Locate every blood parasite and identify its species.
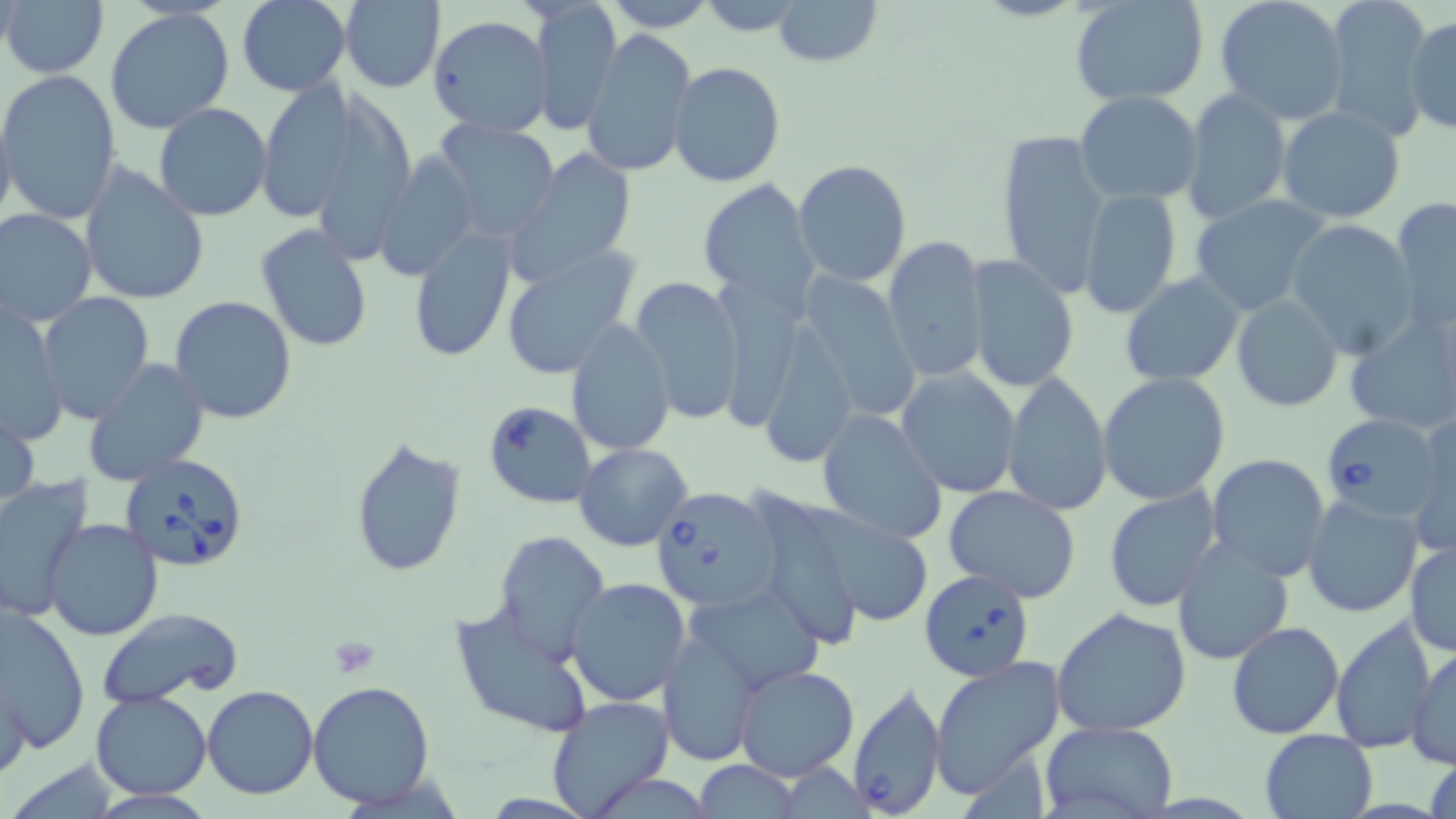

Approximate bounding boxes as (x1, y1, x2, y2) in pixels.
Babesia divergens-infected red blood cells: (1321, 412, 1447, 525), (122, 452, 249, 572), (650, 486, 779, 613), (918, 567, 1036, 684), (848, 682, 947, 818).
No Plasmodium falciparum, Plasmodium ovale, Plasmodium malariae, Plasmodium vivax, or Trypanosoma brucei observed.

slide-level diagnosis = Babesia divergens
modality = light microscopy
uninfected red blood cell locations = approximate bounding boxes as (x1, y1, x2, y2) in pixels: (2, 0, 110, 79), (338, 0, 447, 93), (599, 0, 719, 32), (771, 0, 885, 68), (1214, 0, 1352, 123), (236, 1, 350, 96), (1071, 1, 1209, 105), (1323, 1, 1434, 141), (530, 2, 622, 136), (105, 9, 236, 134), (1403, 13, 1455, 135), (428, 15, 556, 136), (582, 29, 696, 176), (667, 61, 785, 187), (0, 70, 122, 224), (309, 71, 420, 268), (256, 79, 359, 225), (1179, 90, 1293, 226), (1075, 91, 1204, 203), (0, 101, 16, 234), (153, 104, 272, 221), (1276, 106, 1407, 224), (433, 118, 563, 245), (995, 128, 1111, 298), (509, 146, 638, 281), (375, 149, 480, 280), (793, 161, 911, 285), (78, 164, 209, 306), (699, 178, 821, 308), (1079, 187, 1182, 318), (1188, 194, 1335, 315), (1390, 197, 1456, 337), (0, 208, 97, 327), (1286, 219, 1423, 359), (255, 223, 374, 351), (407, 224, 518, 363), (882, 235, 988, 382), (500, 248, 639, 379), (965, 255, 1079, 393), (1121, 271, 1246, 386), (798, 273, 921, 423), (628, 274, 747, 426), (40, 293, 156, 423), (1231, 293, 1344, 411), (170, 295, 296, 425), (2, 302, 67, 449), (1342, 304, 1456, 439), (566, 319, 676, 456), (82, 360, 209, 486), (896, 368, 1020, 497), (1001, 373, 1111, 517), (1097, 374, 1231, 506), (483, 400, 597, 510), (2, 403, 40, 514), (816, 408, 949, 545), (1408, 415, 1456, 558), (351, 435, 467, 578), (574, 442, 692, 550), (1206, 454, 1331, 581), (0, 474, 95, 624), (942, 486, 1082, 601), (1103, 487, 1220, 613), (741, 488, 870, 653), (1302, 493, 1423, 617), (42, 519, 164, 641), (494, 529, 610, 659), (1171, 537, 1294, 667), (1406, 540, 1455, 656), (564, 577, 690, 706), (682, 581, 827, 695), (449, 602, 595, 739), (1, 606, 90, 756), (1050, 606, 1192, 738), (96, 608, 243, 708), (1329, 615, 1440, 754), (1226, 621, 1344, 738), (657, 631, 761, 768), (1407, 645, 1454, 770), (929, 656, 1067, 800), (732, 664, 860, 781), (1, 677, 32, 781), (308, 680, 437, 809), (203, 686, 319, 800), (90, 690, 213, 800), (544, 697, 675, 819), (1039, 720, 1180, 819), (1258, 728, 1380, 819), (1424, 749, 1456, 819), (5, 759, 122, 816), (695, 759, 802, 818)
platelet locations = approximate bounding boxes as (x1, y1, x2, y2) in pixels: (326, 636, 380, 679)
image size = 1456×819 pixels
magnification = 1000x
stain = May-Grünwald-Giemsa
field of view = single
preparation = thin blood smear